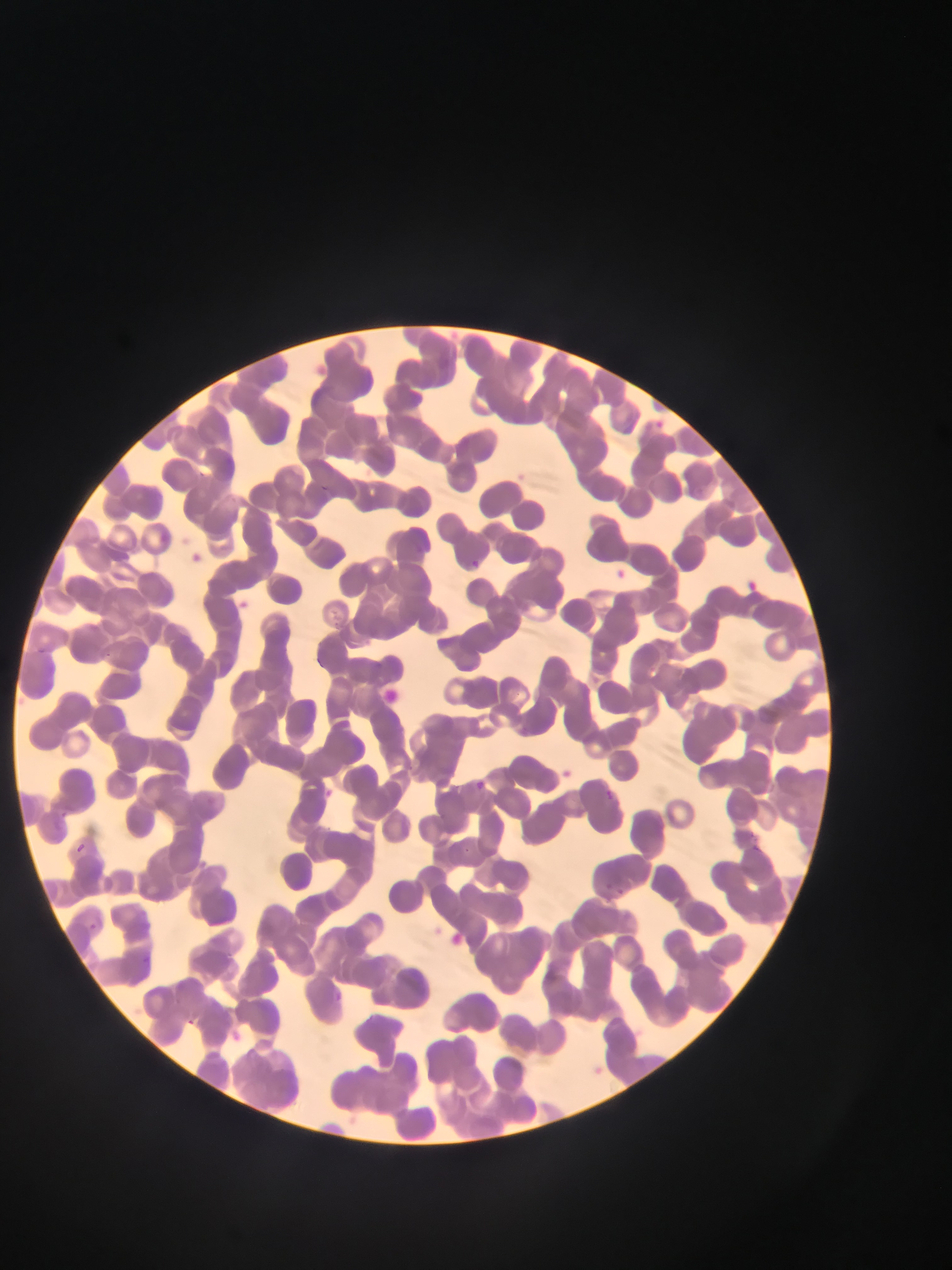

field_of_view: single
country: Ghana
capture: mobile-phone photograph through a microscope
plasmodium_parasite_locations: 'approximate bounding boxes as {left, top, right, bottom} in pixels: {656, 417, 666, 424}, {191, 552, 202, 565}, {472, 559, 484, 573}, {614, 565, 629, 582}, {746, 579, 763, 596}, {474, 775, 491, 791}, {600, 784, 623, 806}, {67, 841, 90, 856}, {752, 842, 765, 854}, {617, 884, 629, 897}, {86, 923, 103, 934}, {188, 1015, 202, 1026}'
image_size: 952×1270 pixels
preparation: thin blood film